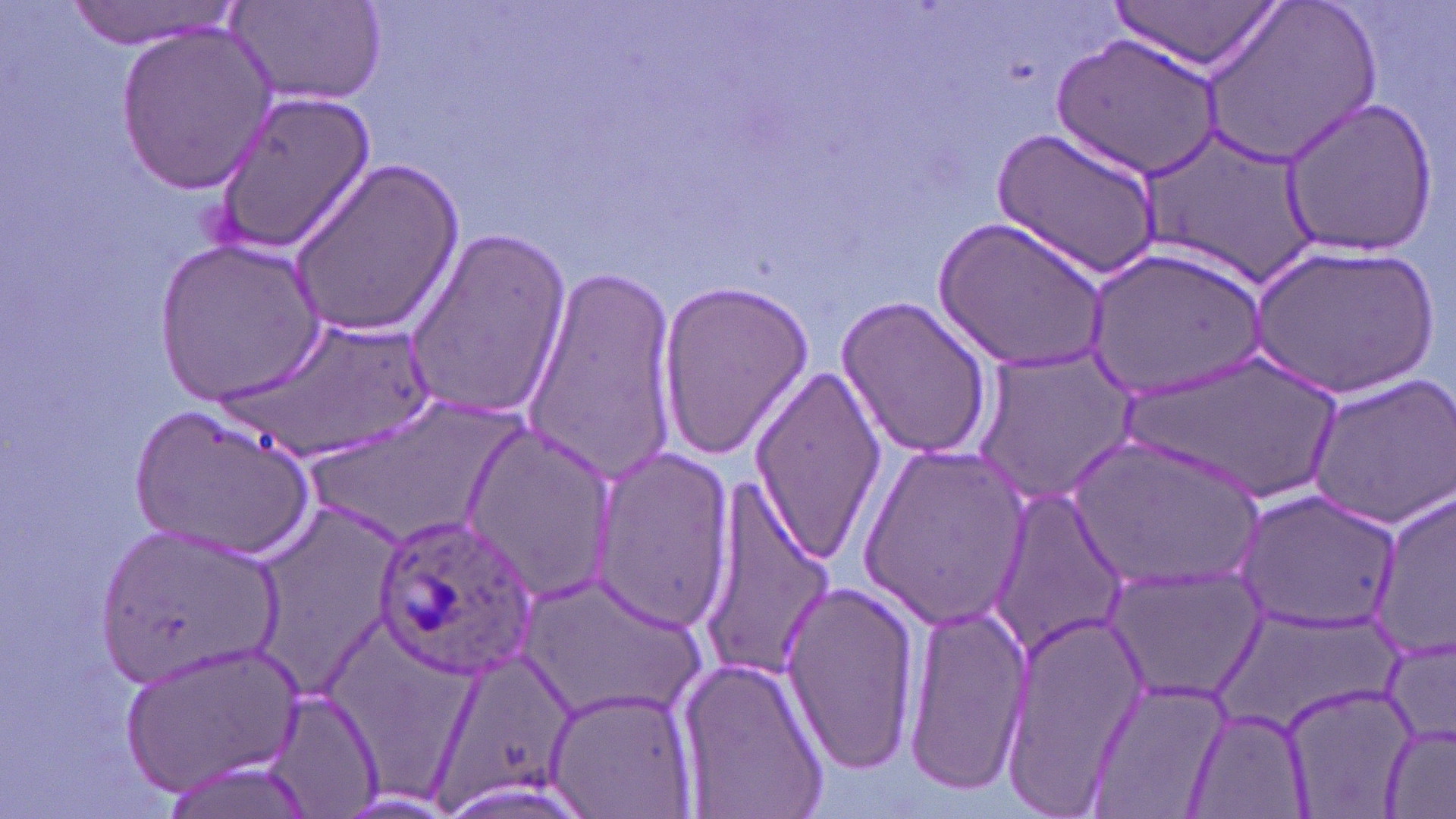

Approximate bounding boxes as [x1, y1, x2, y2] in pixels. Uninfected red blood cell locations: [228, 0, 389, 107], [1197, 0, 1381, 170], [66, 1, 240, 49], [1110, 1, 1280, 76], [116, 23, 275, 193], [1053, 30, 1223, 181], [212, 88, 374, 257], [1278, 97, 1439, 259], [992, 125, 1162, 279], [1142, 126, 1321, 289], [287, 158, 463, 340], [936, 211, 1114, 375], [401, 227, 571, 421], [156, 239, 327, 405], [1248, 243, 1440, 401], [1087, 246, 1270, 401], [517, 261, 678, 481], [654, 276, 814, 460], [837, 295, 995, 462], [221, 317, 443, 460], [969, 346, 1139, 506], [1123, 348, 1348, 503], [748, 362, 884, 565], [1303, 370, 1456, 533], [132, 399, 318, 562], [454, 424, 616, 599], [1067, 431, 1264, 591], [859, 440, 1030, 631], [588, 448, 738, 633], [696, 487, 836, 682], [987, 487, 1128, 659], [1228, 488, 1406, 632], [1368, 488, 1456, 665], [249, 498, 410, 691], [99, 521, 281, 691], [1100, 562, 1264, 703], [521, 569, 707, 727], [776, 579, 924, 773], [900, 599, 1031, 795], [996, 609, 1145, 813], [1380, 630, 1456, 752], [118, 639, 300, 799], [672, 650, 831, 819], [1082, 678, 1231, 816], [1280, 679, 1422, 819], [542, 682, 698, 819], [260, 683, 383, 819], [1186, 709, 1313, 818], [1379, 721, 1455, 819]. Plasmodium ovale-infected red blood cell locations: [374, 515, 537, 681]. Slide-level diagnosis: Plasmodium ovale. Thin blood film. 1000x magnification. Image is 1456×819 pixels. Optical microscopy. May-Grünwald-Giemsa-stained preparation. Single field of view.